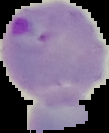
Cell region segmented out of the field of view; the surrounding area is masked to black. Result: Plasmodium parasites detected. From a thin blood film. Image is 109×133 pixels.